Identify the cell.
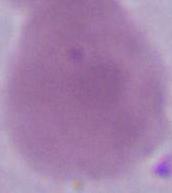

This is an erythrocyte.

modality = micrograph
magnification = 1000x